Name the blood parasite species.
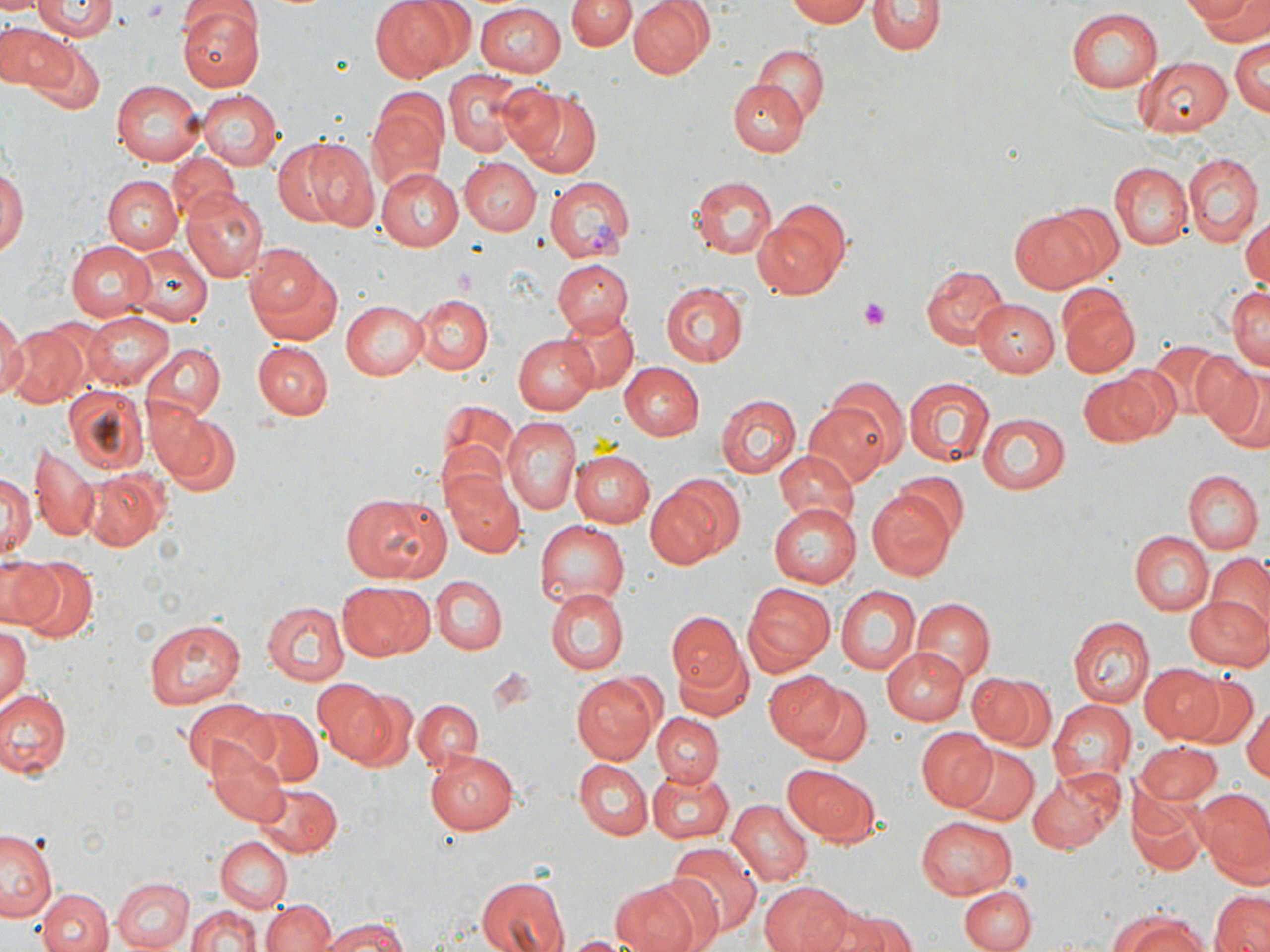
Plasmodium vivax.

Approximate bounding boxes as [x1, y1, x2, y2] in pixels. Uninfected red blood cell locations: [0, 0, 41, 18], [176, 0, 266, 93], [371, 0, 463, 81], [568, 0, 632, 52], [627, 0, 713, 79], [785, 0, 871, 27], [1190, 0, 1269, 42], [868, 1, 942, 55], [30, 2, 118, 41], [474, 5, 565, 76], [1065, 9, 1163, 92], [0, 19, 65, 91], [1229, 36, 1269, 117], [30, 42, 105, 115], [753, 43, 829, 123], [1133, 56, 1232, 137], [444, 70, 529, 157], [109, 80, 202, 167], [729, 81, 806, 156], [496, 82, 569, 158], [517, 88, 600, 176], [199, 89, 282, 171], [367, 89, 447, 194], [279, 137, 372, 230], [169, 152, 238, 219], [1182, 153, 1260, 247], [461, 157, 540, 234], [0, 162, 27, 261], [1111, 162, 1192, 249], [374, 168, 463, 250], [100, 175, 180, 253], [689, 176, 778, 259], [182, 187, 268, 282], [1042, 201, 1127, 283], [754, 203, 849, 296], [1008, 209, 1104, 295], [1243, 214, 1270, 294], [64, 239, 154, 320], [124, 243, 212, 326], [245, 244, 339, 339], [552, 259, 633, 334], [920, 263, 1007, 351], [660, 282, 749, 365], [1227, 283, 1270, 373], [1059, 291, 1140, 376], [412, 295, 491, 374], [973, 297, 1061, 377], [341, 299, 428, 380], [555, 310, 638, 395], [84, 311, 175, 391], [0, 315, 25, 400], [4, 321, 93, 408], [517, 332, 601, 415], [252, 340, 333, 418], [1148, 341, 1234, 421], [139, 342, 225, 423], [1195, 357, 1266, 444], [619, 363, 703, 439], [1077, 372, 1164, 447], [904, 375, 994, 467], [826, 376, 908, 466], [64, 386, 148, 474], [717, 394, 800, 478], [804, 399, 896, 486], [436, 401, 518, 497], [156, 412, 241, 496], [976, 413, 1069, 495], [503, 417, 580, 515], [30, 448, 101, 540], [569, 448, 653, 528], [775, 449, 860, 530], [0, 467, 35, 563], [82, 468, 168, 549], [442, 469, 524, 557], [898, 472, 970, 541], [1184, 472, 1260, 552], [646, 478, 738, 568], [432, 480, 583, 571], [867, 489, 956, 581], [342, 492, 451, 582], [769, 505, 860, 588], [533, 520, 627, 612], [1129, 530, 1213, 615], [1204, 555, 1270, 639], [1, 556, 64, 631], [18, 559, 96, 642], [431, 575, 506, 655], [336, 580, 431, 662], [740, 583, 835, 674], [834, 585, 921, 677], [547, 587, 628, 673], [1184, 594, 1270, 672], [913, 597, 994, 684], [262, 601, 349, 687], [667, 613, 747, 698], [1068, 616, 1153, 708], [142, 618, 246, 708], [0, 624, 29, 713], [883, 647, 968, 723], [672, 650, 754, 723], [1140, 665, 1224, 742], [762, 671, 844, 751], [966, 672, 1053, 750], [570, 674, 658, 765], [1179, 677, 1256, 749], [311, 678, 390, 763], [789, 683, 873, 768], [0, 688, 71, 781], [339, 688, 419, 769], [179, 696, 279, 777], [412, 698, 482, 771], [1048, 699, 1136, 789], [1244, 703, 1270, 781], [238, 710, 325, 785], [653, 714, 725, 787], [916, 729, 998, 811], [207, 741, 289, 825], [1134, 743, 1222, 804], [950, 745, 1039, 826], [424, 749, 517, 834], [575, 758, 651, 840], [784, 765, 876, 843], [646, 768, 735, 842], [1027, 769, 1124, 854], [247, 781, 343, 858], [1195, 789, 1270, 880], [1129, 792, 1204, 878], [726, 800, 811, 888], [916, 815, 1018, 900], [2, 829, 60, 923], [216, 837, 292, 910], [667, 840, 763, 939], [113, 876, 195, 951], [475, 876, 569, 952], [608, 878, 707, 952], [758, 881, 850, 952], [959, 885, 1035, 952], [36, 887, 111, 952], [1212, 891, 1270, 952], [263, 899, 335, 952], [186, 902, 263, 952], [832, 909, 914, 952], [1105, 911, 1214, 952], [318, 916, 412, 952], [558, 934, 644, 952]. Platelet locations: [861, 300, 889, 330]. Plasmodium vivax-infected red blood cell locations: [544, 177, 636, 262]. Thin blood smear. Image is 1270×952 pixels. Optical microscopy. 1000x magnification. One field of a larger specimen. May-Grünwald-Giemsa stain.